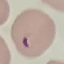 Malaria status: parasitized. Automatically extracted cell patch, resized to 64 × 64 pixels. Thin blood film. Acquired by smartphone through the microscope eyepiece. Giemsa-stained preparation.